Identify the cell.
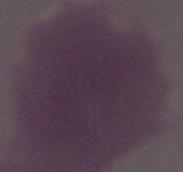

An erythrocyte.

{
  "magnification": "1000x",
  "modality": "photomicrograph"
}